Evaluate for Plasmodium parasites.
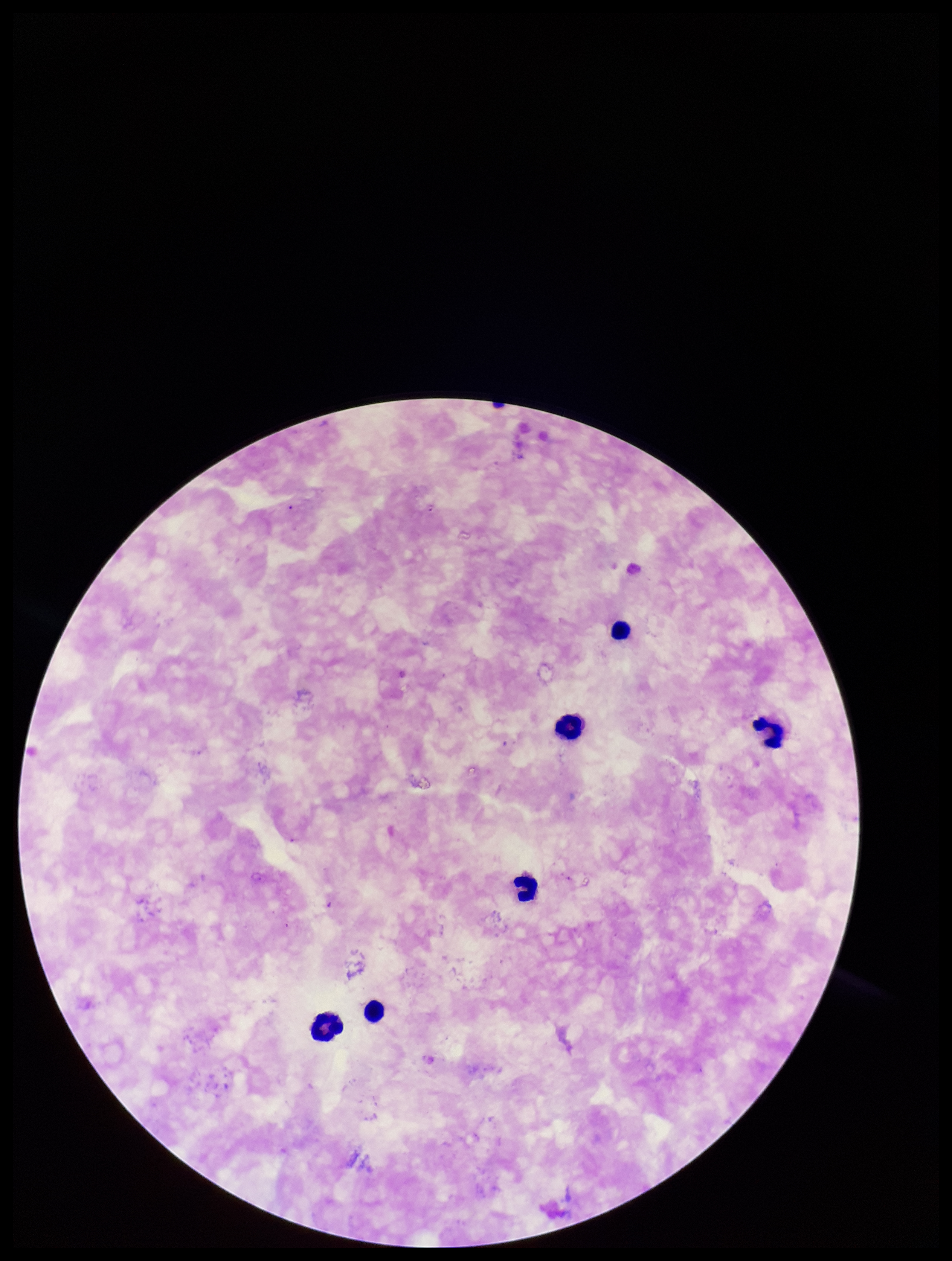

None seen.

Summary:
  - Field of view: one from this slide
  - Stain: Giemsa
  - Capture: smartphone photograph through the microscope eyepiece
  - Image size: 952×1261 pixels
  - Patient malaria status: negative
  - Preparation: thick
  - Parasite count: 0
  - Leukocyte count: 6